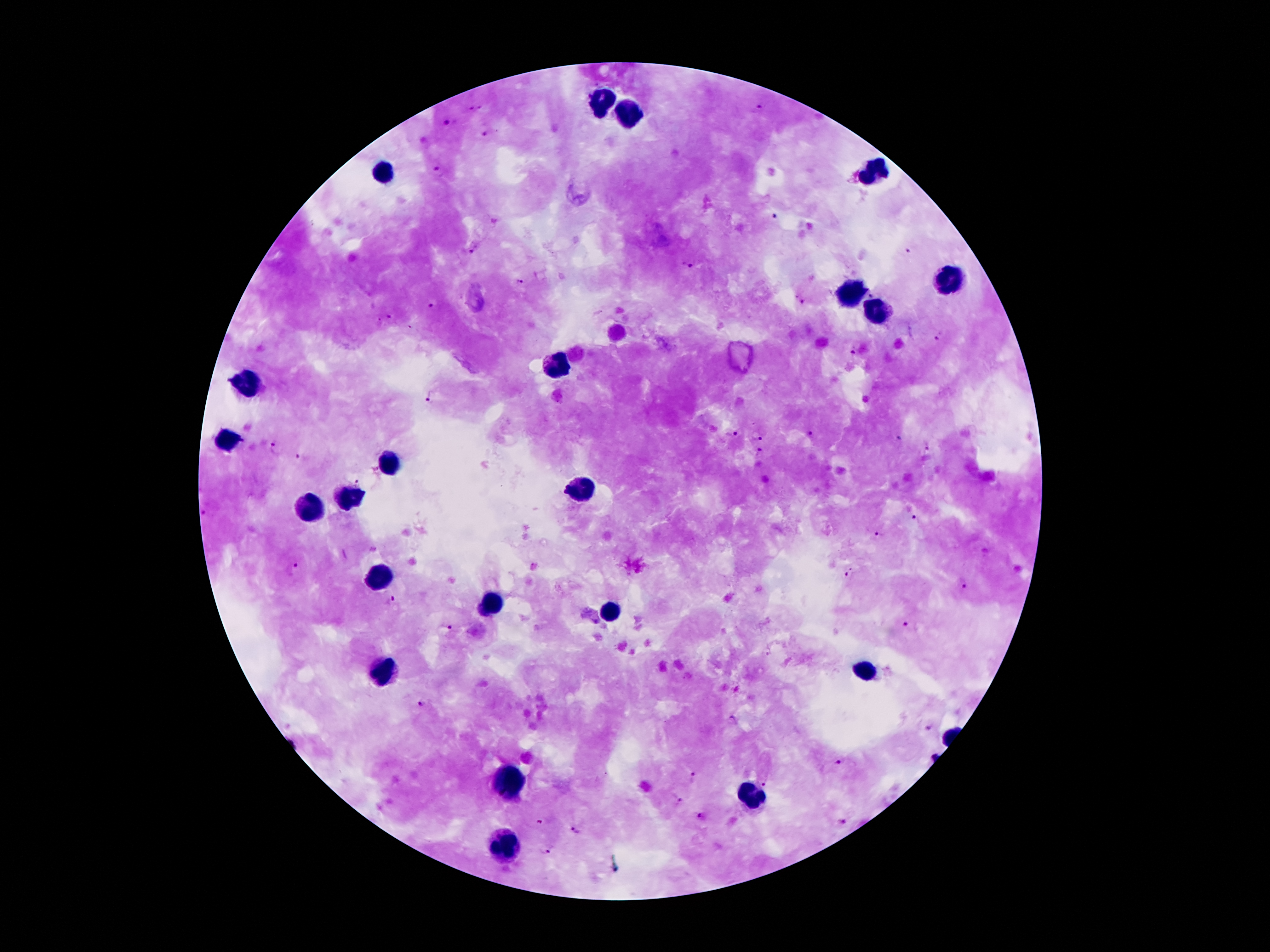
magnification: 100x
stain: Giemsa
image_size: 1270×952 pixels
capture: smartphone camera through the microscope eyepiece
leukocyte_locations: 'approximate centers as [x, y] in pixels: [604, 103], [628, 113], [874, 172], [385, 175], [948, 280], [851, 295], [877, 312], [559, 365], [246, 384], [229, 441], [388, 462], [583, 490], [347, 499], [310, 505], [378, 575], [488, 603], [611, 612], [866, 670], [386, 671], [509, 783], [751, 799], [506, 846]'
patient_malaria_status: infected with Plasmodium falciparum
plasmodium_parasite_locations: 'approximate centers as [x, y] in pixels: [475, 108], [759, 109], [446, 122], [484, 133], [438, 171], [772, 216], [473, 249], [907, 250], [686, 265], [518, 282], [799, 298], [431, 307], [390, 318], [938, 339], [854, 352], [430, 398], [732, 434], [809, 435], [757, 436], [896, 438], [926, 446], [277, 447], [758, 452], [301, 457], [357, 484], [205, 514], [915, 520], [878, 534], [294, 568], [850, 572], [962, 584], [391, 601], [908, 626], [450, 629], [422, 702], [731, 719], [928, 728], [840, 762], [693, 776], [763, 782], [677, 799], [701, 816], [841, 821], [576, 829], [544, 848]'
preparation: thick peripheral-blood smear
field_of_view: one from this slide